Describe the morphology of the erythrocytes.
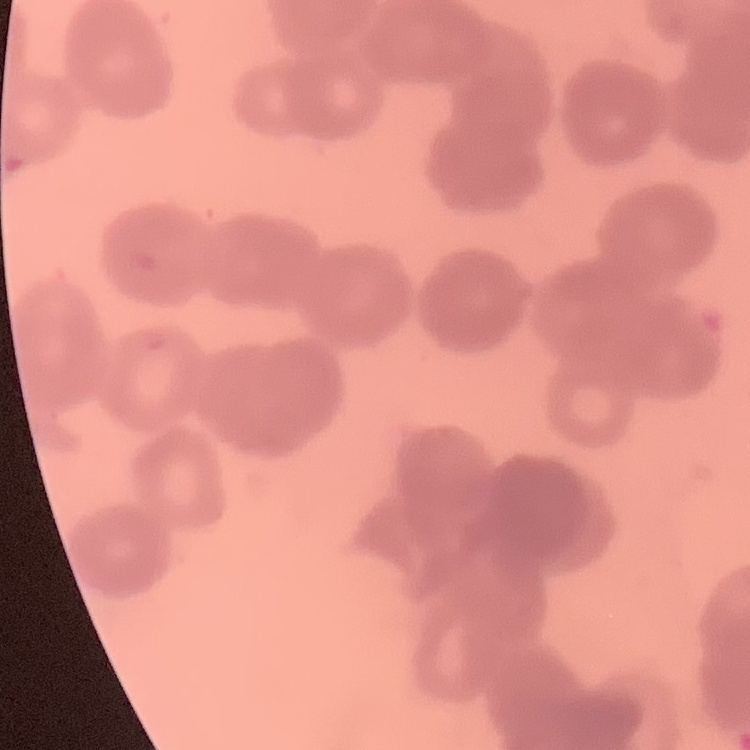

Rouleaux formation.

One tile cut from a larger photomicrograph. Thin blood smear. Field's or Giemsa stain.